State which cell type is depicted.
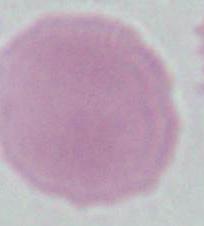
This is an erythrocyte.

magnification = 1000x
modality = micrograph